Assess this cell for malaria.
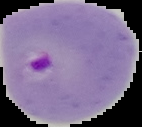

Parasitized.

Summary:
  - Preparation: thin blood smear
  - Image type: segmented cell region with the area outside set to black
  - Image size: 142×127 pixels